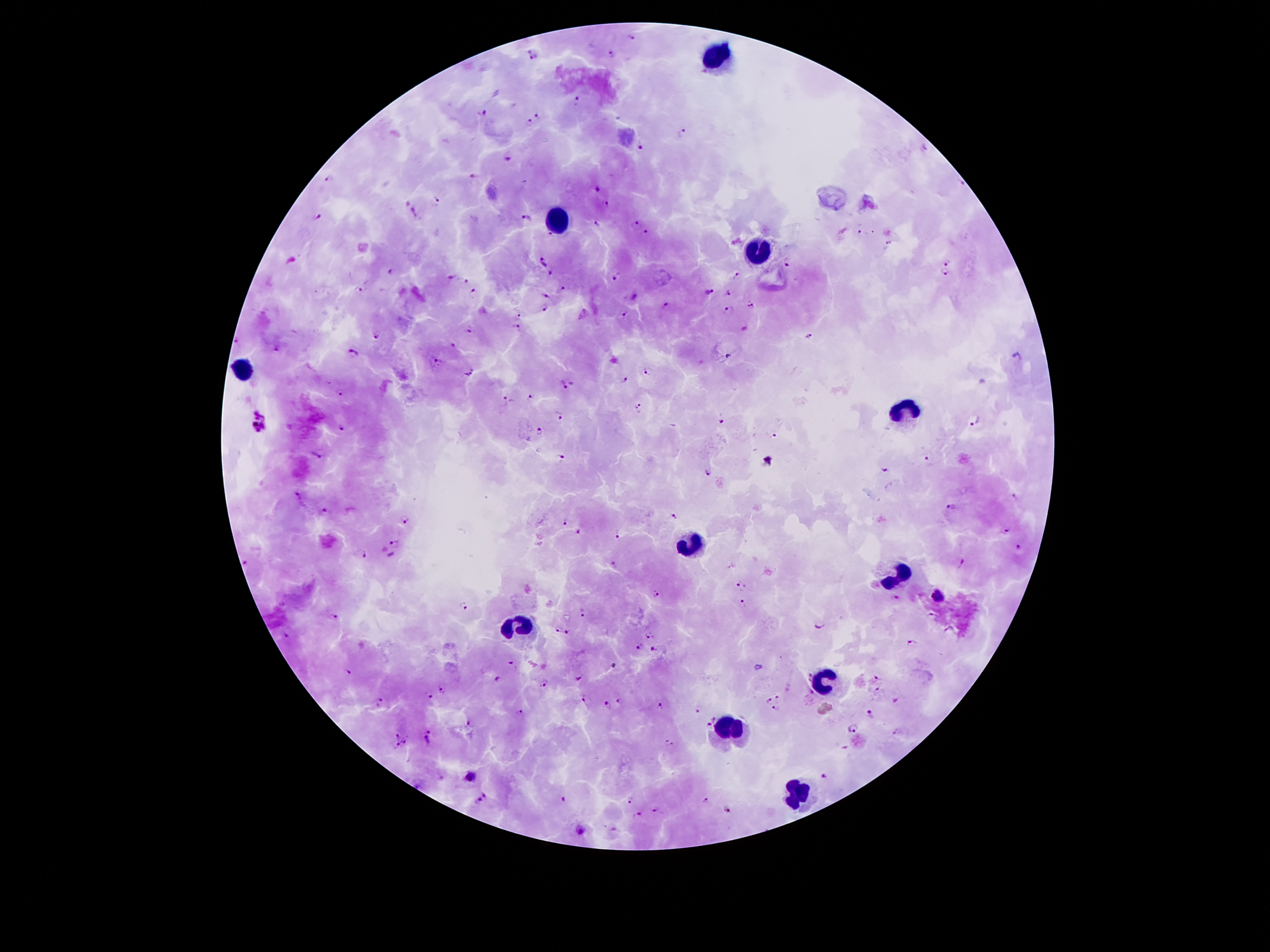
Approximate centers as (x, y) in pixels. Plasmodium parasite locations: (633, 36), (611, 54), (533, 57), (578, 101), (482, 113), (537, 116), (619, 118), (528, 121), (682, 133), (642, 145), (926, 147), (507, 159), (474, 175), (328, 179), (960, 185), (597, 189), (437, 199), (605, 203), (413, 209), (317, 216), (524, 216), (417, 218), (595, 223), (634, 223), (859, 230), (549, 232), (871, 232), (647, 233), (889, 244), (542, 262), (788, 262), (949, 262), (551, 271), (390, 272), (945, 273), (451, 276), (737, 276), (615, 277), (467, 280), (364, 289), (561, 289), (709, 292), (472, 293), (728, 293), (545, 295), (633, 295), (667, 305), (750, 305), (543, 308), (728, 310), (623, 315), (517, 316), (517, 327), (744, 327), (470, 329), (807, 335), (376, 337), (278, 347), (453, 347), (352, 354), (729, 356), (433, 360), (648, 371), (468, 373), (625, 380), (569, 385), (339, 394), (532, 396), (504, 401), (639, 407), (559, 417), (720, 420), (974, 420), (260, 424), (342, 429), (539, 432), (772, 436), (318, 454), (559, 457), (928, 458), (769, 459), (886, 472), (707, 473), (296, 494), (1017, 499), (950, 506), (325, 512), (673, 515), (404, 520), (564, 523), (1004, 530), (580, 533), (616, 537), (394, 544), (1015, 548), (364, 553), (392, 556), (244, 562), (962, 565), (612, 566), (742, 584), (654, 595), (938, 597), (895, 598), (741, 602), (464, 607), (583, 612), (931, 614), (337, 616), (818, 625), (559, 630), (568, 631), (650, 634), (287, 635), (912, 642), (640, 646), (654, 651), (514, 664), (613, 664), (758, 665), (349, 671), (808, 675), (580, 676), (878, 678), (496, 679), (544, 684), (442, 689), (876, 689), (429, 694), (777, 697), (585, 699), (620, 700), (769, 700), (896, 700), (379, 701), (607, 704), (660, 705), (775, 708), (697, 711), (519, 713), (869, 713), (713, 718), (467, 724), (707, 726), (853, 729), (896, 731), (429, 732), (396, 734), (425, 741), (405, 742), (670, 743), (396, 745), (823, 776), (471, 777), (486, 795), (563, 798), (706, 799), (478, 800), (630, 801), (726, 810), (654, 811), (638, 815), (580, 831). Leukocyte locations: (720, 55), (556, 213), (756, 248), (243, 370), (903, 408), (690, 545), (895, 570), (516, 626), (827, 681), (727, 726), (795, 790). Giemsa stain. Thick blood smear. 100x magnification. Image is 1270×952 pixels. Single field of view. Patient malaria status: positive for Plasmodium falciparum. Photographed through the microscope eyepiece with a smartphone camera.